Assess this cell for malaria.
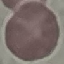
Uninfected.

preparation = thin blood film
capture = smartphone camera at the microscope eyepiece
stain = Giemsa
image type = automatically extracted cell patch, resized to 64 × 64 pixels